Locate and identify every blood parasite.
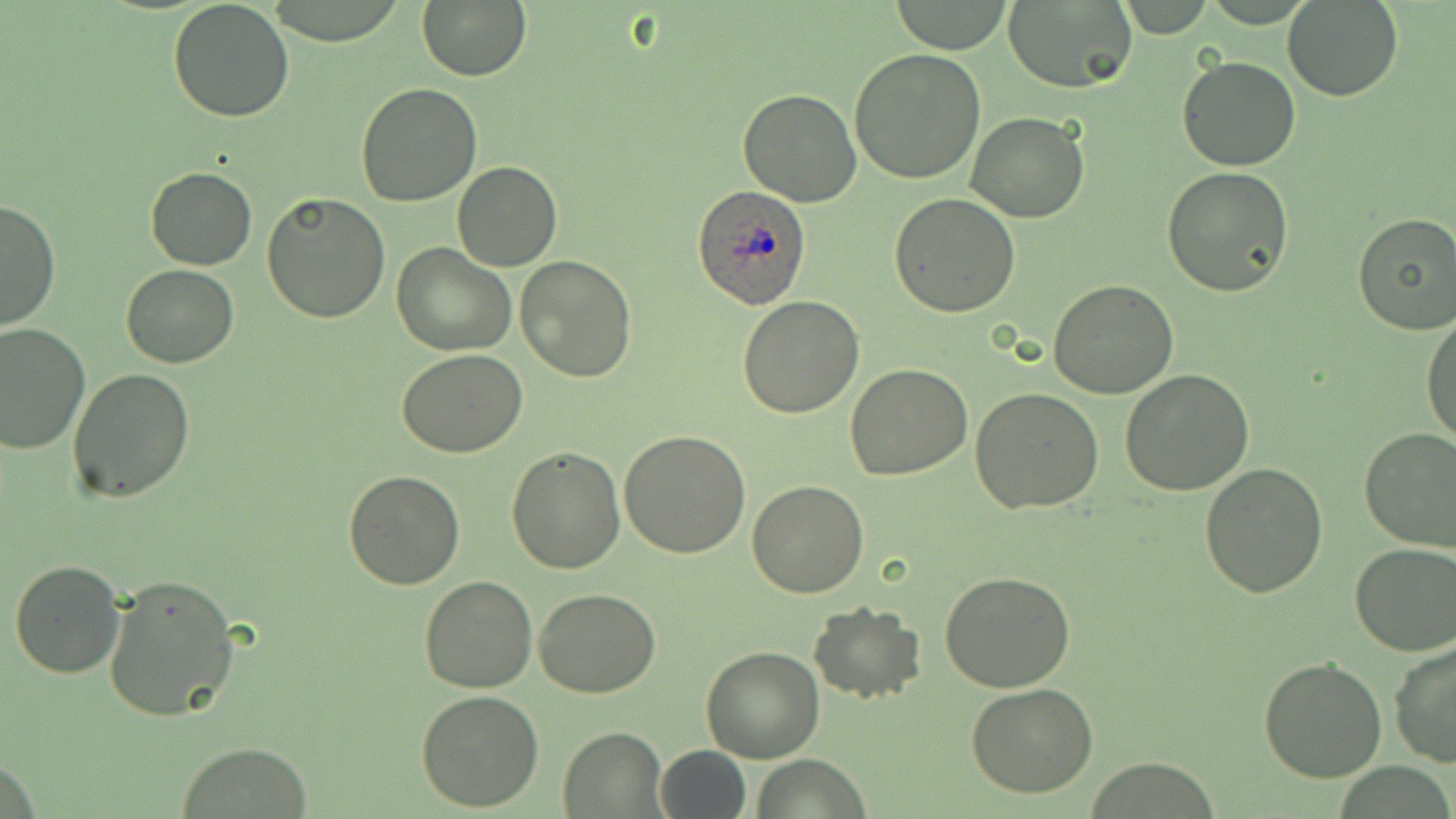
Approximate bounding boxes as [x1, y1, x2, y2] in pixels.
Plasmodium ovale-infected red blood cells: [692, 185, 811, 310].
No Plasmodium falciparum, Plasmodium malariae, Plasmodium vivax, Babesia divergens, or Trypanosoma brucei observed.

Summary:
  - Uninfected red blood cell locations: [168, 0, 294, 120], [266, 0, 411, 47], [416, 0, 532, 82], [889, 0, 1015, 54], [1282, 0, 1402, 101], [1003, 2, 1136, 92], [849, 46, 986, 184], [1175, 56, 1302, 172], [356, 83, 483, 207], [736, 89, 862, 207], [965, 111, 1090, 223], [452, 161, 561, 271], [1161, 166, 1294, 298], [145, 167, 258, 270], [261, 192, 390, 322], [890, 193, 1020, 316], [0, 199, 60, 331], [1352, 212, 1456, 334], [392, 243, 514, 355], [515, 255, 637, 384], [119, 264, 239, 366], [1047, 280, 1178, 400], [737, 295, 864, 419], [1421, 313, 1455, 449], [0, 322, 91, 453], [0, 337, 178, 473], [397, 348, 529, 457], [844, 365, 972, 481], [68, 368, 197, 503], [1120, 370, 1254, 495], [971, 387, 1104, 515], [1359, 428, 1456, 553], [618, 430, 751, 558], [507, 445, 627, 573], [1200, 463, 1327, 597], [343, 470, 465, 590], [747, 481, 868, 598], [1349, 543, 1456, 657], [9, 558, 125, 678], [940, 572, 1076, 694], [103, 573, 240, 723], [419, 575, 538, 693], [534, 587, 661, 697], [808, 603, 926, 703], [1389, 642, 1456, 769], [700, 645, 825, 764], [1259, 658, 1386, 781], [967, 684, 1098, 799], [416, 689, 545, 810], [558, 728, 665, 816], [177, 742, 312, 817], [653, 745, 751, 819], [753, 756, 871, 818]
  - Slide-level diagnosis: Plasmodium ovale
  - Field of view: single
  - Stain: May-Grünwald-Giemsa
  - Preparation: thin blood smear
  - Magnification: 1000x
  - Image size: 1456×819 pixels
  - Modality: light microscopy